Classify this cell by malaria status.
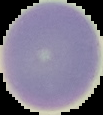
Uninfected.

preparation: thin blood film
image_type: segmented cell region with the area outside set to black
image_size: 103×115 pixels